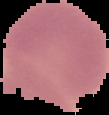
{
  "image_type": "segmented cell region on a black background",
  "image_size": "109×115 pixels",
  "malaria_status": "uninfected",
  "preparation": "thin blood smear"
}